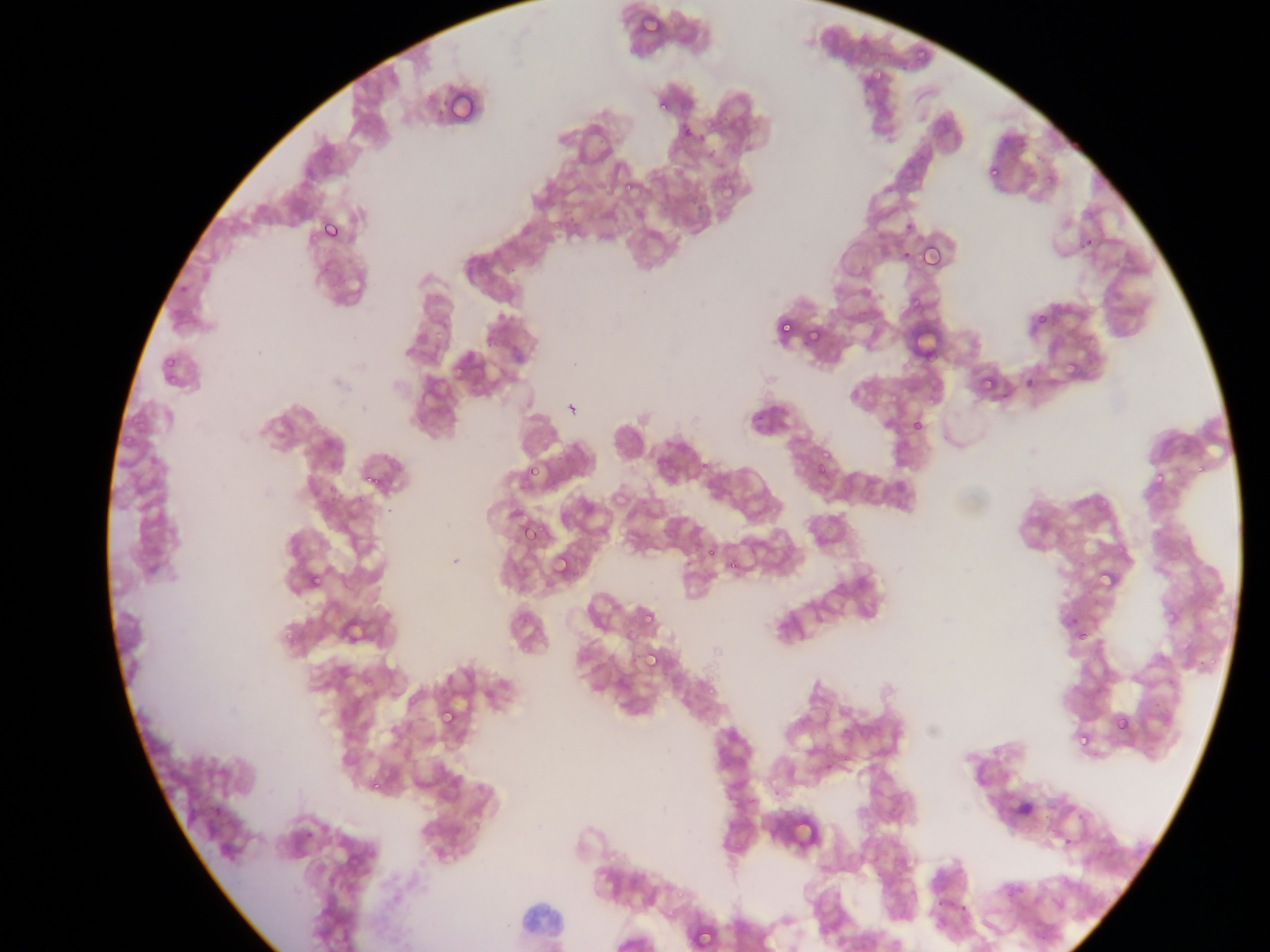
image size = 1270×952 pixels
field of view = single
capture = mobile-phone photograph through a microscope
Plasmodium parasite locations = approximate bounding boxes as {left, top, right, bottom} in pixels: {638, 12, 663, 38}, {913, 44, 932, 64}, {868, 68, 885, 82}, {657, 101, 673, 115}, {988, 165, 1002, 180}, {714, 182, 734, 202}, {620, 184, 631, 192}, {902, 212, 915, 227}, {317, 218, 343, 247}, {918, 241, 945, 273}, {896, 252, 906, 267}, {912, 295, 927, 310}, {1036, 312, 1050, 326}, {778, 319, 796, 338}, {810, 332, 822, 343}, {162, 358, 174, 369}, {1062, 360, 1077, 374}, {978, 370, 998, 394}, {167, 374, 182, 384}, {909, 416, 926, 435}, {816, 446, 829, 463}, {1193, 457, 1211, 476}, {522, 461, 544, 486}, {1152, 461, 1172, 484}, {812, 462, 831, 481}, {361, 463, 389, 494}, {520, 520, 545, 545}, {703, 546, 718, 563}, {550, 551, 576, 579}, {725, 556, 743, 575}, {1096, 573, 1116, 590}, {309, 576, 322, 589}, {641, 607, 654, 628}, {1067, 613, 1083, 629}, {1075, 631, 1089, 641}, {285, 633, 300, 646}, {641, 648, 663, 673}, {705, 683, 719, 695}, {437, 705, 459, 730}, {1112, 715, 1132, 735}, {1074, 738, 1087, 748}, {367, 776, 387, 795}, {211, 805, 227, 822}, {675, 879, 688, 896}, {690, 922, 717, 951}
preparation = thin blood film
country = Ghana